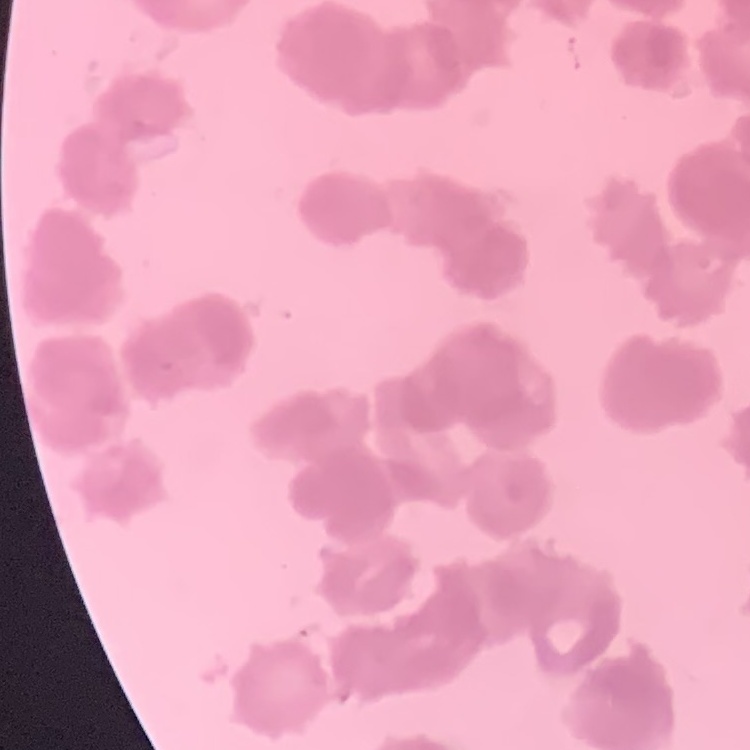 The red blood cells show rouleaux formation. Thin blood smear. One tile cut from a larger photomicrograph. Stained with either Field's or Giemsa.